Identify the cell.
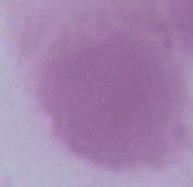
An erythrocyte.

1000x magnification. Micrograph.